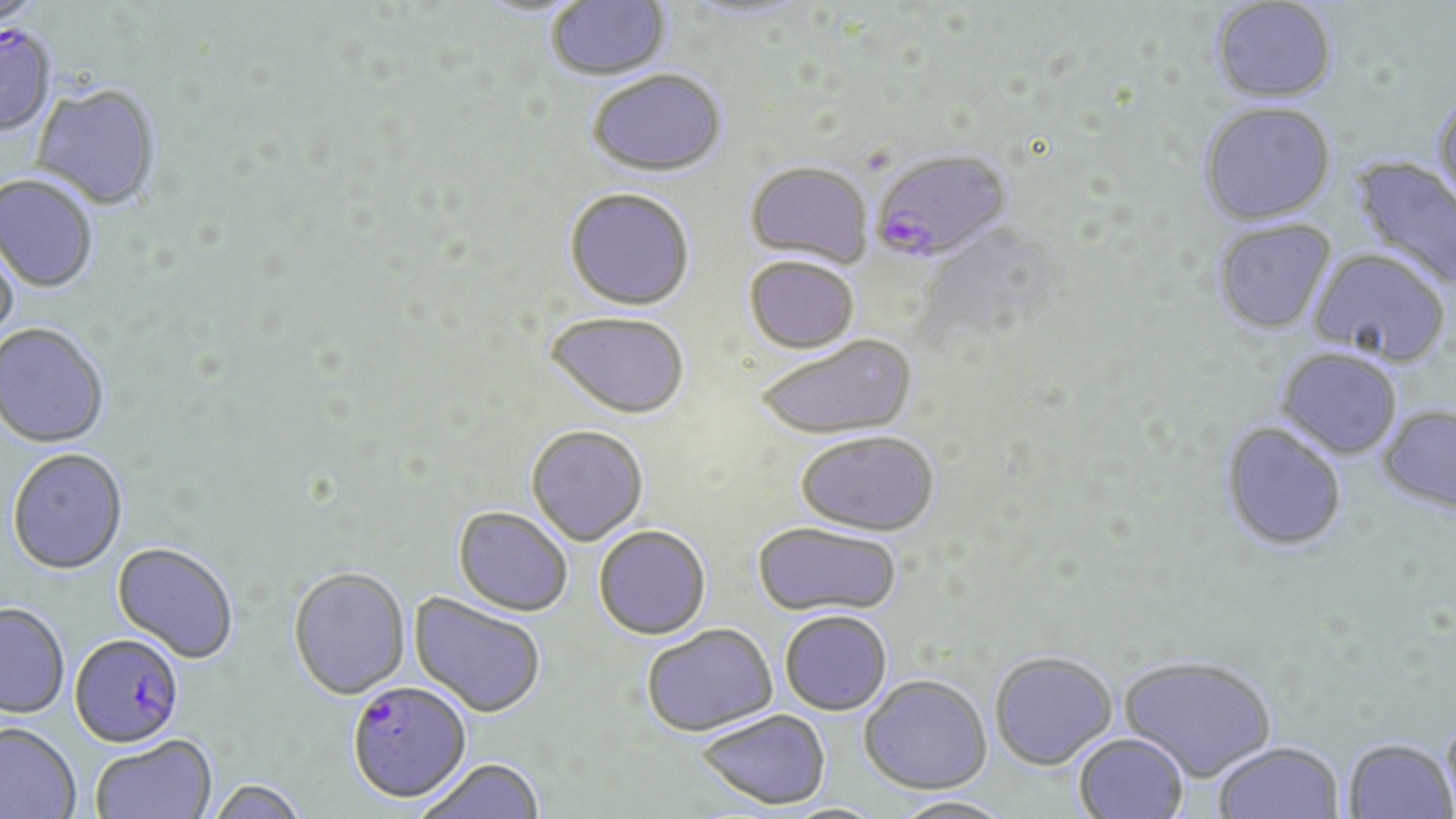

Summary:
  - Coordinate format: approximate bounding boxes as (x1, y1, x2, y2) in pixels
  - Uninfected red blood cell locations: (546, 0, 670, 80), (1210, 1, 1339, 106), (588, 68, 727, 176), (31, 85, 161, 212), (1433, 91, 1456, 220), (1199, 103, 1336, 228), (1349, 155, 1456, 295), (745, 160, 874, 268), (0, 175, 98, 294), (564, 187, 695, 310), (1212, 220, 1337, 337), (0, 227, 22, 354), (1308, 250, 1450, 369), (743, 255, 858, 354), (544, 311, 690, 418), (0, 324, 110, 449), (754, 335, 918, 440), (1276, 349, 1403, 461), (1378, 406, 1456, 516), (1219, 423, 1347, 553), (526, 424, 649, 545), (795, 431, 939, 536), (7, 448, 128, 574), (454, 506, 573, 616), (752, 521, 902, 618), (593, 525, 710, 638), (113, 541, 239, 662), (288, 566, 410, 698), (409, 592, 546, 718), (0, 603, 69, 717), (779, 609, 893, 715), (641, 623, 777, 735), (989, 650, 1117, 769), (1119, 655, 1276, 781), (859, 674, 991, 794), (696, 708, 831, 809), (1442, 712, 1456, 818), (0, 722, 81, 819), (1073, 732, 1189, 819), (90, 734, 217, 819), (1343, 739, 1455, 819), (1213, 741, 1344, 819), (415, 758, 545, 819), (208, 778, 308, 819), (892, 795, 1015, 819)
  - Plasmodium falciparum-infected red blood cell locations: (0, 26, 57, 138), (870, 148, 1012, 263), (69, 633, 184, 747), (347, 681, 471, 803)
  - Slide-level diagnosis: Plasmodium falciparum
  - Preparation: thin blood film
  - Stain: May-Grünwald-Giemsa
  - Image size: 1456×819 pixels
  - Magnification: 1000x
  - Modality: light microscopy
  - Field of view: single